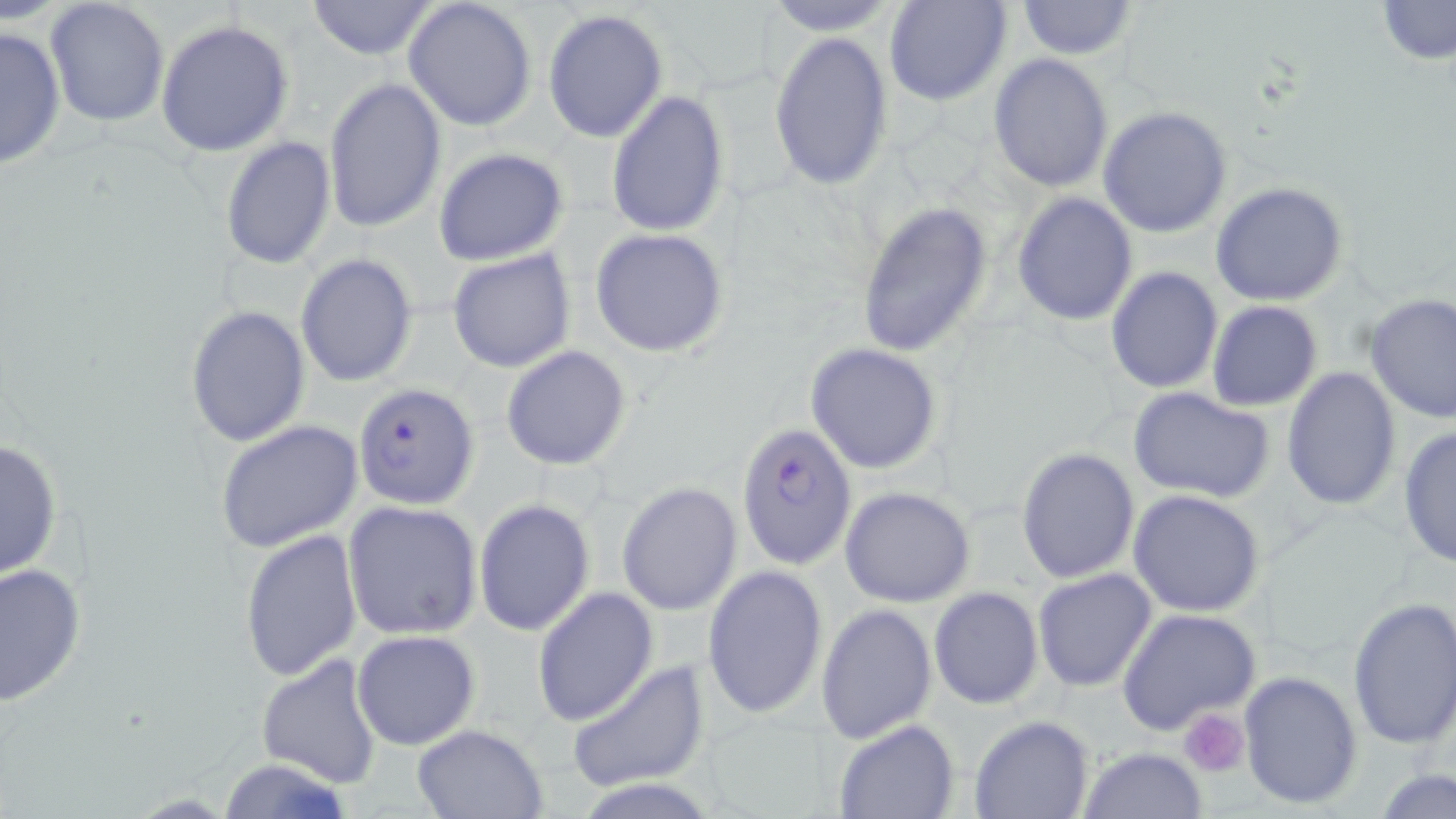
Approximate bounding boxes as (x1, y1, x2, y2) in pixels. Platelet locations: (1178, 708, 1252, 778). Uninfected red blood cell locations: (303, 0, 440, 60), (402, 0, 538, 132), (759, 0, 904, 34), (884, 0, 1012, 107), (1014, 0, 1139, 59), (1374, 0, 1456, 65), (43, 1, 171, 129), (543, 10, 668, 142), (156, 19, 295, 157), (0, 25, 67, 171), (768, 31, 894, 190), (988, 54, 1114, 193), (323, 76, 447, 233), (606, 90, 730, 236), (1097, 106, 1233, 238), (219, 137, 337, 271), (432, 147, 568, 267), (1210, 181, 1350, 306), (1012, 191, 1140, 325), (856, 200, 994, 360), (588, 227, 731, 359), (446, 249, 576, 373), (296, 253, 418, 388), (1105, 264, 1223, 394), (1363, 293, 1456, 423), (1207, 300, 1324, 412), (185, 304, 311, 448), (805, 341, 943, 475), (501, 345, 632, 470), (1281, 366, 1401, 510), (1127, 386, 1278, 504), (215, 419, 366, 555), (1396, 425, 1455, 567), (0, 438, 63, 581), (1015, 446, 1141, 583), (616, 482, 743, 615), (840, 487, 976, 607), (1127, 489, 1266, 616), (473, 500, 595, 637), (341, 501, 483, 639), (239, 527, 363, 680), (0, 561, 87, 707), (702, 563, 829, 721), (1032, 567, 1157, 692), (929, 586, 1044, 710), (531, 587, 657, 727), (1346, 594, 1456, 748), (816, 603, 937, 744), (1117, 608, 1259, 733), (354, 630, 479, 750), (256, 653, 384, 786), (563, 660, 709, 792), (1238, 670, 1363, 811), (969, 716, 1092, 819), (832, 719, 959, 819), (410, 723, 550, 818), (1077, 746, 1208, 819), (210, 757, 362, 818), (1374, 768, 1455, 818). Plasmodium falciparum-infected red blood cell locations: (355, 382, 480, 507), (736, 421, 858, 570). Slide-level diagnosis: Plasmodium falciparum. Image is 1456×819 pixels. May-Grünwald-Giemsa stain. Captured at 1000x magnification. Optical microscopy. Thin blood smear. One field of a larger specimen.